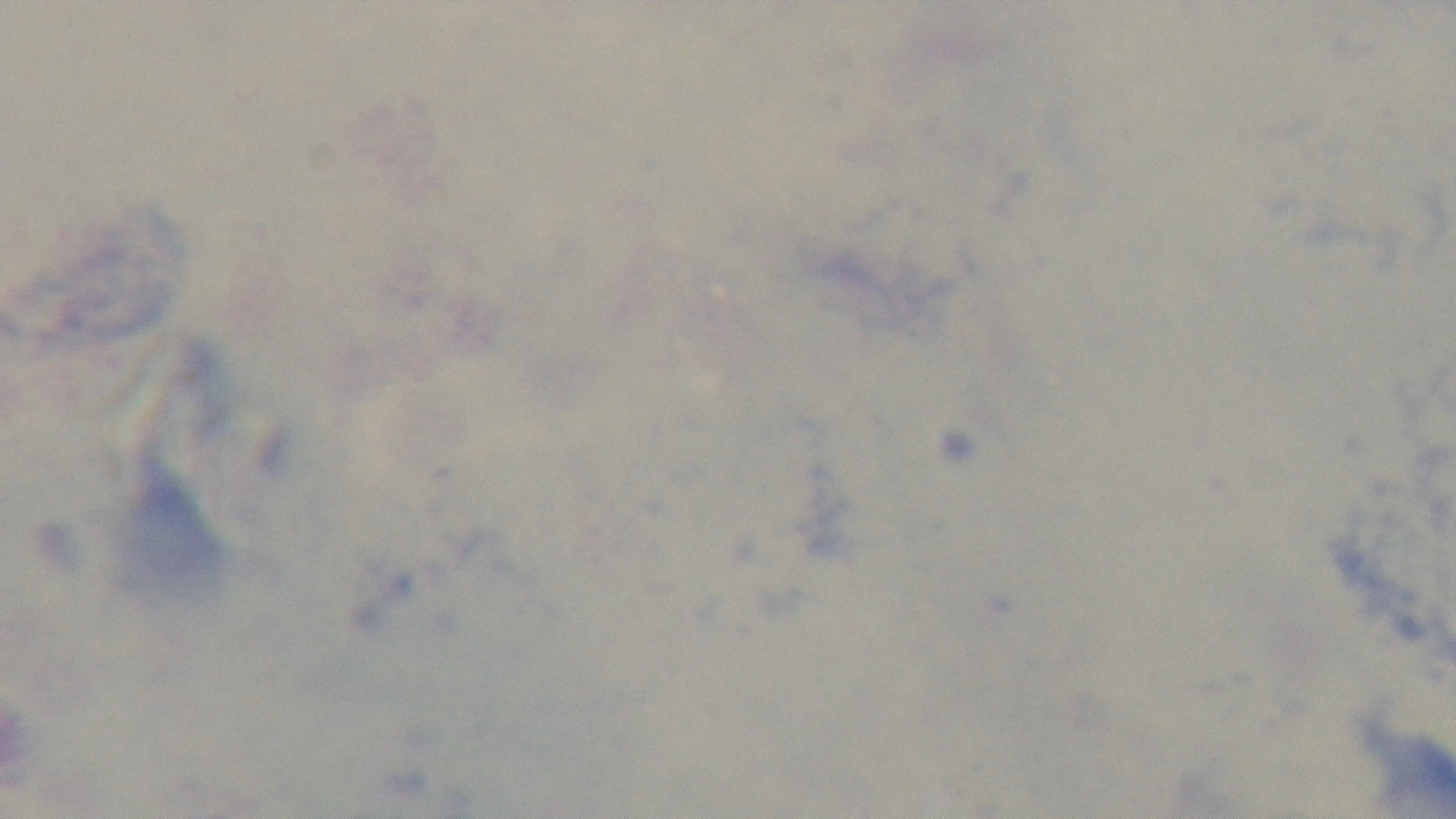 100x oil-immersion objective. Malaria status: negative. Giemsa stain. Mounted 4K digital camera. Light microscopy. One field from the slide. Preparation: thick smear.